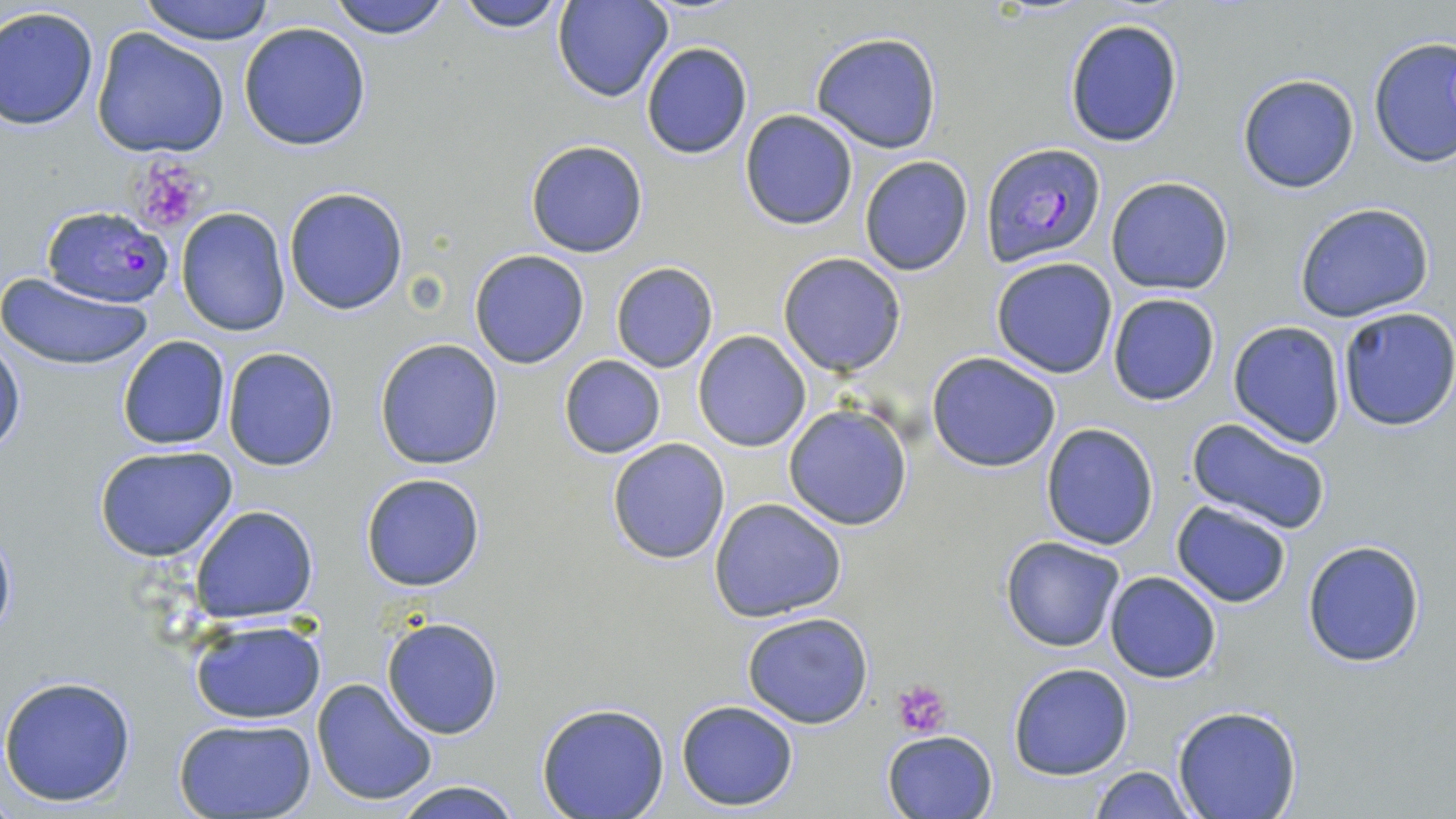

Summary:
  - Coordinate format: approximate bounding boxes as (x1,y1)-(x2,y2) corner pairs in pixels
  - Plasmodium falciparum-infected red blood cell locations: (983,144)-(1105,268), (41,204)-(172,309)
  - Uninfected red blood cell locations: (137,0)-(277,44), (325,0)-(455,39), (454,0)-(573,32), (552,1)-(673,104), (0,6)-(100,131), (1062,17)-(1185,148), (239,21)-(372,151), (90,27)-(230,159), (809,31)-(943,154), (1368,37)-(1455,170), (640,42)-(753,159), (1237,74)-(1360,193), (738,109)-(858,230), (524,139)-(651,259), (859,156)-(974,276), (1105,175)-(1237,296), (283,186)-(411,315), (1293,202)-(1436,322), (175,206)-(291,337), (469,250)-(591,368), (777,252)-(908,376), (991,257)-(1118,379), (610,262)-(718,372), (0,273)-(153,371), (1106,293)-(1220,407), (1335,307)-(1456,431), (1227,320)-(1345,449), (693,331)-(812,451), (0,333)-(25,457), (117,335)-(231,451), (374,338)-(505,470), (222,346)-(339,471), (927,352)-(1063,473), (558,355)-(667,459), (783,404)-(914,531), (1184,416)-(1334,535), (1040,423)-(1160,550), (606,438)-(730,564), (94,444)-(239,562), (360,472)-(487,592), (710,497)-(847,622), (1171,501)-(1291,607), (190,504)-(319,624), (0,523)-(17,643), (1001,537)-(1127,653), (1301,538)-(1427,668), (1103,570)-(1222,683), (741,611)-(875,729), (380,615)-(506,740), (189,617)-(326,724), (1008,662)-(1133,780), (0,675)-(138,808), (312,677)-(437,807), (674,699)-(800,810), (536,703)-(670,819), (1172,707)-(1303,819), (172,717)-(317,819), (882,730)-(999,819), (1089,765)-(1194,819), (385,778)-(528,819)
  - Platelet locations: (128,157)-(211,235), (894,679)-(952,739)
  - Slide-level diagnosis: Plasmodium falciparum
  - Image size: 1456×819 pixels
  - Preparation: thin blood smear
  - Magnification: 1000x
  - Stain: May-Grünwald-Giemsa
  - Modality: optical microscopy
  - Field of view: single